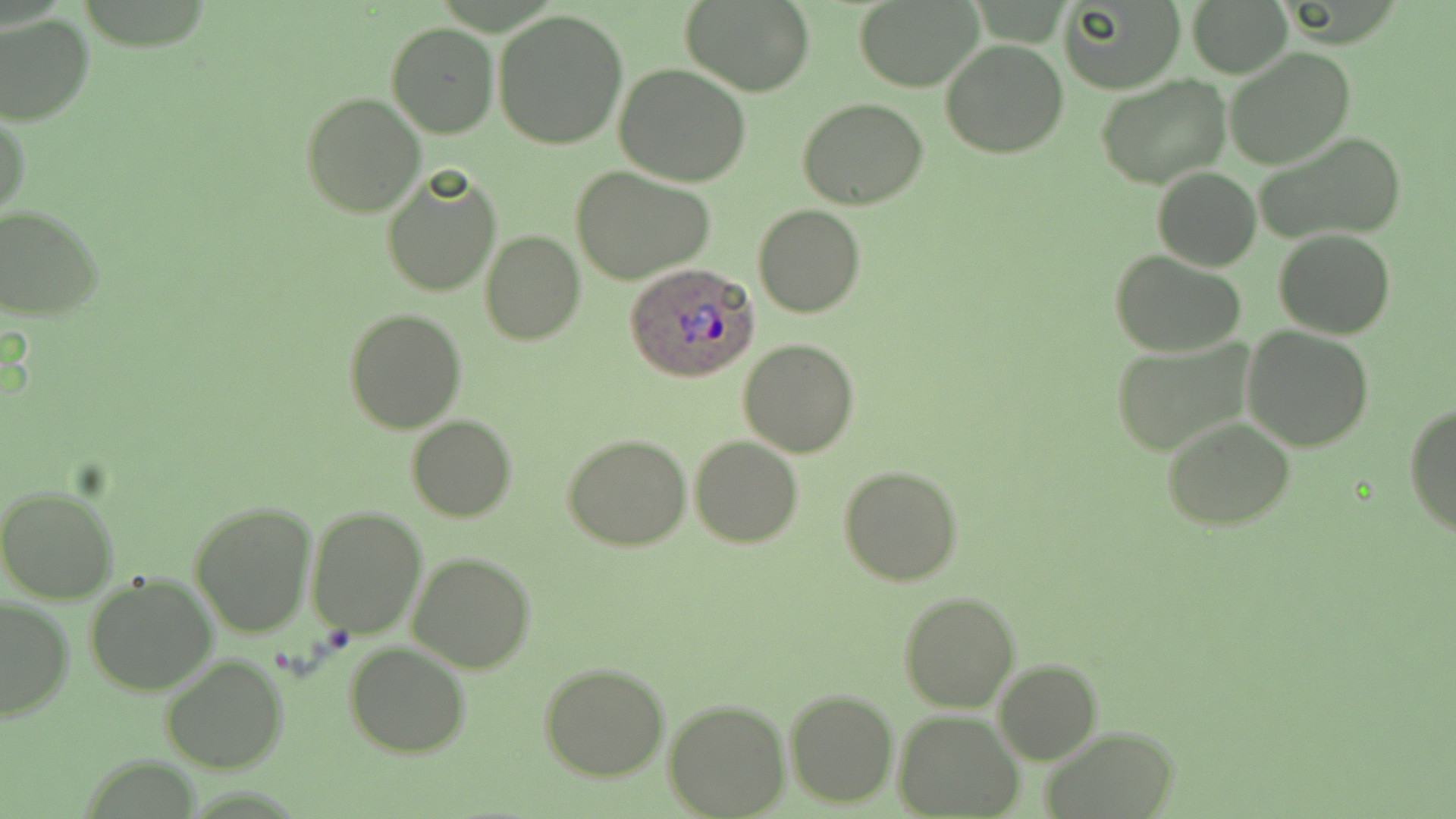

Summary:
  - Coordinate format: approximate bounding boxes as named x1/y1/x2/y2 corners in pixels
  - Uninfected red blood cell locations: (x1=854, y1=0, x2=986, y2=92), (x1=1059, y1=0, x2=1186, y2=94), (x1=1187, y1=0, x2=1294, y2=77), (x1=680, y1=1, x2=814, y2=96), (x1=493, y1=9, x2=628, y2=151), (x1=0, y1=14, x2=94, y2=126), (x1=387, y1=23, x2=499, y2=138), (x1=941, y1=39, x2=1068, y2=159), (x1=1225, y1=47, x2=1356, y2=170), (x1=614, y1=63, x2=751, y2=187), (x1=1096, y1=72, x2=1232, y2=188), (x1=300, y1=91, x2=425, y2=216), (x1=798, y1=98, x2=928, y2=209), (x1=1, y1=107, x2=30, y2=225), (x1=1252, y1=131, x2=1407, y2=247), (x1=569, y1=164, x2=717, y2=284), (x1=380, y1=167, x2=502, y2=298), (x1=1152, y1=167, x2=1261, y2=271), (x1=753, y1=203, x2=865, y2=318), (x1=0, y1=206, x2=104, y2=321), (x1=1274, y1=229, x2=1395, y2=340), (x1=481, y1=231, x2=584, y2=345), (x1=1111, y1=250, x2=1246, y2=358), (x1=343, y1=307, x2=467, y2=434), (x1=1242, y1=327, x2=1375, y2=451), (x1=738, y1=338, x2=858, y2=457), (x1=1110, y1=338, x2=1256, y2=457), (x1=1405, y1=403, x2=1456, y2=538), (x1=406, y1=416, x2=516, y2=522), (x1=1162, y1=417, x2=1296, y2=532), (x1=563, y1=434, x2=692, y2=551), (x1=689, y1=436, x2=803, y2=548), (x1=838, y1=464, x2=963, y2=586), (x1=0, y1=487, x2=120, y2=604), (x1=190, y1=499, x2=318, y2=638), (x1=305, y1=505, x2=428, y2=639), (x1=406, y1=552, x2=536, y2=674), (x1=84, y1=572, x2=220, y2=697), (x1=899, y1=591, x2=1019, y2=712), (x1=0, y1=597, x2=74, y2=722), (x1=344, y1=642, x2=472, y2=759), (x1=160, y1=653, x2=289, y2=773), (x1=993, y1=660, x2=1102, y2=765), (x1=538, y1=662, x2=669, y2=781), (x1=784, y1=688, x2=898, y2=808), (x1=662, y1=698, x2=790, y2=818), (x1=894, y1=711, x2=1023, y2=818), (x1=1043, y1=725, x2=1177, y2=818)
  - Plasmodium ovale-infected red blood cell locations: (x1=624, y1=261, x2=762, y2=383)
  - Slide-level diagnosis: Plasmodium ovale
  - Field of view: single
  - Image size: 1456×819 pixels
  - Preparation: thin blood film
  - Stain: May-Grünwald-Giemsa
  - Modality: light microscopy
  - Magnification: 1000x